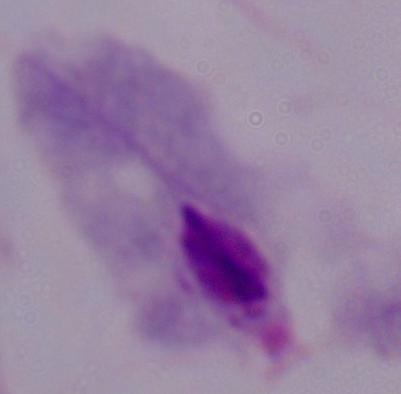 Micrograph. Captured at 1000x magnification. A trichomonad is seen.